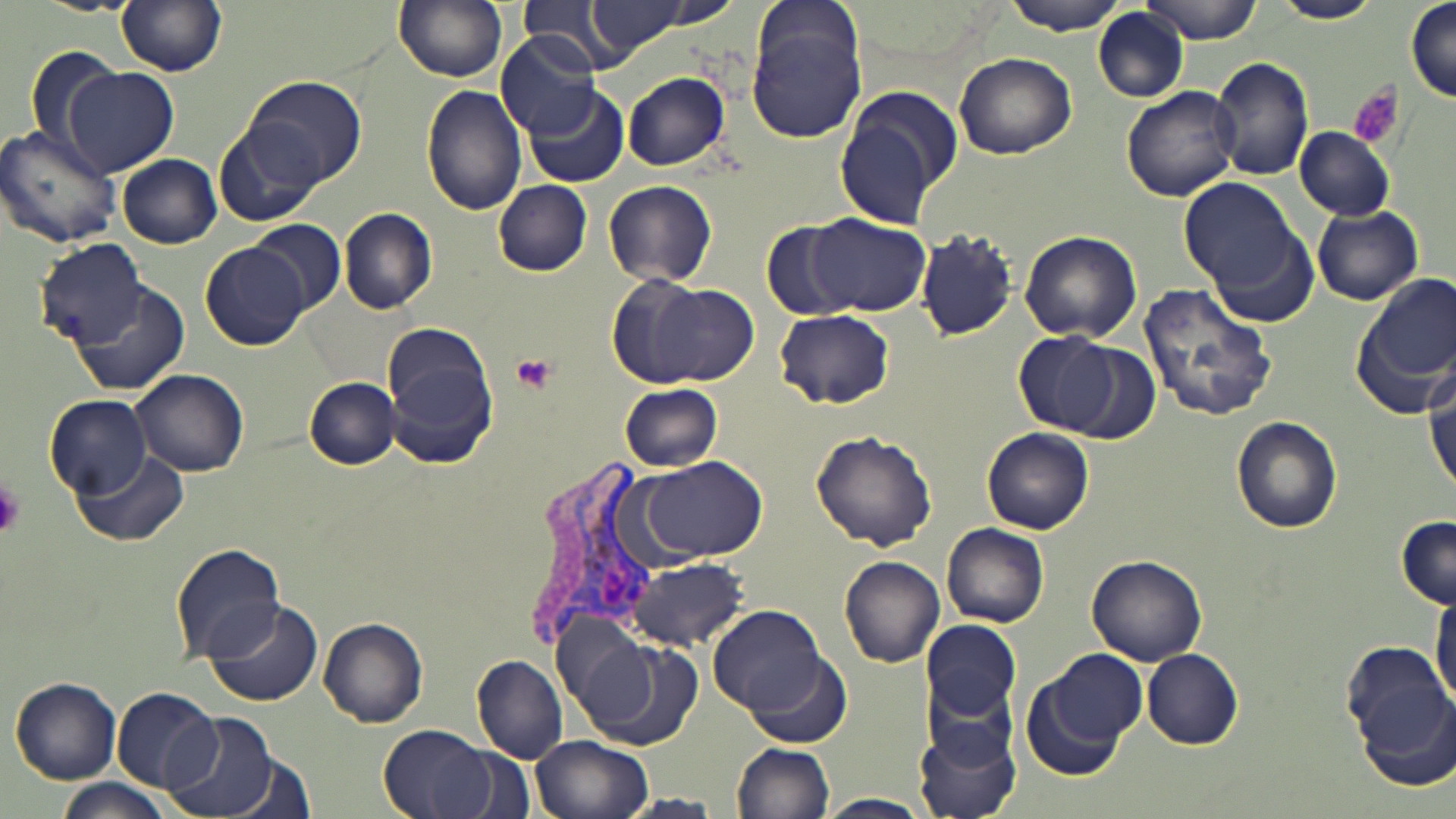 Approximate bounding boxes as named x1/y1/x2/y2 corners in pixels. Uninfected red blood cell locations: (x1=392, y1=0, x2=508, y2=84), (x1=576, y1=0, x2=699, y2=60), (x1=1003, y1=0, x2=1131, y2=35), (x1=1141, y1=0, x2=1265, y2=44), (x1=1273, y1=0, x2=1380, y2=24), (x1=116, y1=1, x2=227, y2=76), (x1=519, y1=1, x2=627, y2=74), (x1=1406, y1=2, x2=1456, y2=105), (x1=745, y1=4, x2=869, y2=145), (x1=1093, y1=7, x2=1190, y2=105), (x1=498, y1=32, x2=605, y2=143), (x1=24, y1=42, x2=126, y2=158), (x1=954, y1=52, x2=1077, y2=160), (x1=1210, y1=56, x2=1315, y2=182), (x1=60, y1=67, x2=178, y2=177), (x1=622, y1=71, x2=730, y2=171), (x1=242, y1=73, x2=366, y2=187), (x1=421, y1=84, x2=527, y2=217), (x1=1120, y1=85, x2=1241, y2=203), (x1=525, y1=86, x2=632, y2=187), (x1=833, y1=93, x2=958, y2=230), (x1=214, y1=120, x2=326, y2=228), (x1=0, y1=123, x2=122, y2=248), (x1=1297, y1=126, x2=1396, y2=219), (x1=118, y1=153, x2=223, y2=248), (x1=494, y1=179, x2=592, y2=276), (x1=1180, y1=179, x2=1299, y2=292), (x1=604, y1=180, x2=719, y2=288), (x1=1312, y1=204, x2=1424, y2=306), (x1=340, y1=207, x2=440, y2=314), (x1=804, y1=214, x2=930, y2=318), (x1=1203, y1=218, x2=1322, y2=329), (x1=251, y1=221, x2=347, y2=314), (x1=760, y1=221, x2=854, y2=320), (x1=914, y1=228, x2=1017, y2=340), (x1=1020, y1=230, x2=1142, y2=344), (x1=37, y1=240, x2=150, y2=346), (x1=201, y1=243, x2=310, y2=349), (x1=606, y1=274, x2=753, y2=390), (x1=1357, y1=274, x2=1456, y2=403), (x1=73, y1=281, x2=190, y2=396), (x1=1134, y1=282, x2=1279, y2=425), (x1=776, y1=308, x2=894, y2=411), (x1=380, y1=323, x2=501, y2=468), (x1=1015, y1=332, x2=1121, y2=436), (x1=1063, y1=341, x2=1161, y2=444), (x1=133, y1=369, x2=250, y2=476), (x1=304, y1=378, x2=401, y2=470), (x1=619, y1=383, x2=723, y2=472), (x1=1428, y1=393, x2=1455, y2=497), (x1=46, y1=395, x2=151, y2=498), (x1=1232, y1=416, x2=1344, y2=534), (x1=982, y1=429, x2=1095, y2=535), (x1=809, y1=430, x2=937, y2=551), (x1=75, y1=450, x2=188, y2=546), (x1=638, y1=456, x2=766, y2=561), (x1=1396, y1=516, x2=1455, y2=609), (x1=943, y1=523, x2=1049, y2=628), (x1=170, y1=541, x2=286, y2=663), (x1=1086, y1=554, x2=1207, y2=666), (x1=625, y1=557, x2=749, y2=651), (x1=840, y1=557, x2=945, y2=668), (x1=1431, y1=586, x2=1456, y2=710), (x1=202, y1=597, x2=324, y2=709), (x1=707, y1=604, x2=824, y2=719), (x1=317, y1=618, x2=428, y2=728), (x1=558, y1=620, x2=707, y2=755), (x1=922, y1=620, x2=1022, y2=721), (x1=1339, y1=639, x2=1449, y2=754), (x1=746, y1=648, x2=851, y2=746), (x1=1142, y1=649, x2=1244, y2=749), (x1=1019, y1=651, x2=1147, y2=781), (x1=471, y1=653, x2=569, y2=763), (x1=11, y1=677, x2=123, y2=783), (x1=1355, y1=679, x2=1456, y2=793), (x1=922, y1=680, x2=1019, y2=769), (x1=112, y1=688, x2=224, y2=793), (x1=165, y1=712, x2=283, y2=819), (x1=915, y1=722, x2=1023, y2=819), (x1=379, y1=724, x2=501, y2=819), (x1=528, y1=735, x2=657, y2=819), (x1=732, y1=741, x2=836, y2=819), (x1=432, y1=742, x2=536, y2=819), (x1=224, y1=754, x2=318, y2=819), (x1=55, y1=777, x2=176, y2=819), (x1=817, y1=792, x2=932, y2=817), (x1=620, y1=793, x2=723, y2=817). Platelet locations: (x1=1348, y1=81, x2=1404, y2=149), (x1=510, y1=353, x2=558, y2=395), (x1=0, y1=481, x2=25, y2=537). Plasmodium vivax-infected red blood cell locations: (x1=519, y1=461, x2=658, y2=661). Slide-level diagnosis: Plasmodium vivax. Thin blood film. Captured at 1000x magnification. May-Grünwald-Giemsa stain. One field of a larger specimen. Optical microscopy. Image is 1456×819 pixels.